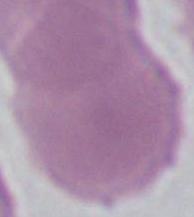
Summary:
  - Magnification: 1000x
  - Modality: micrograph
  - Identification: erythrocyte